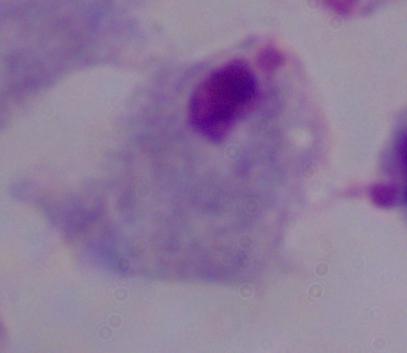
Summary:
  - Identification: trichomonad
  - Magnification: 1000x
  - Modality: micrograph